Assess this cell for malaria.
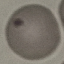

Parasitized.

Giemsa stain. Thin blood film. Automatically extracted cell patch, resized to 64 × 64 pixels. Photographed with a smartphone camera at the microscope eyepiece.